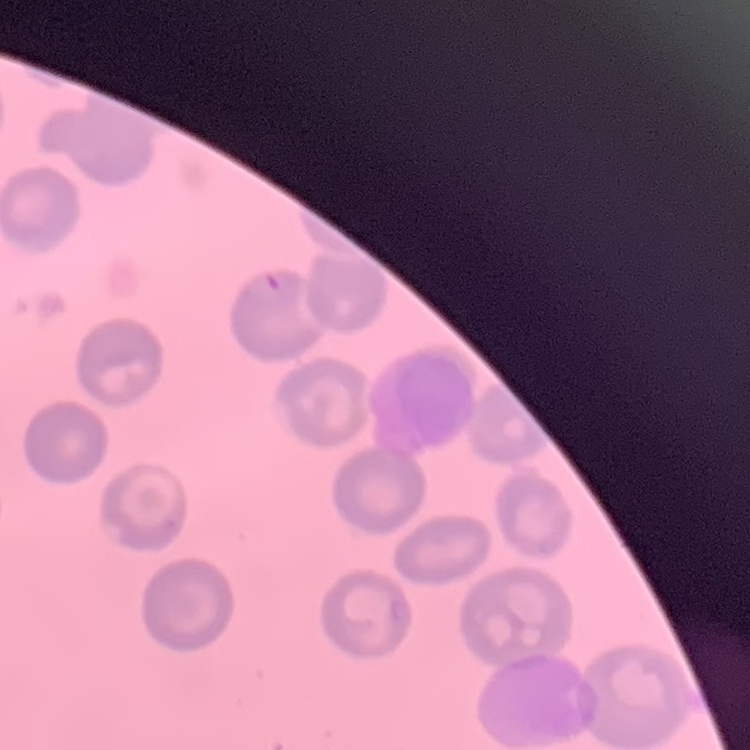

The erythrocytes show no rouleaux formation. Thin blood film. Field's or Giemsa stain. Square crop of a larger photomicrograph.